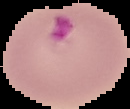

image size = 130×109 pixels
preparation = thin blood film
image type = segmented cell region on a black background
result = Plasmodium parasites identified